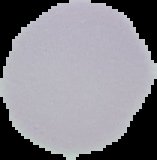

Image is 157×160 pixels. Result: no malaria parasites detected. Cell region segmented out of the field of view; the surrounding area is masked to black. From a thin blood smear.